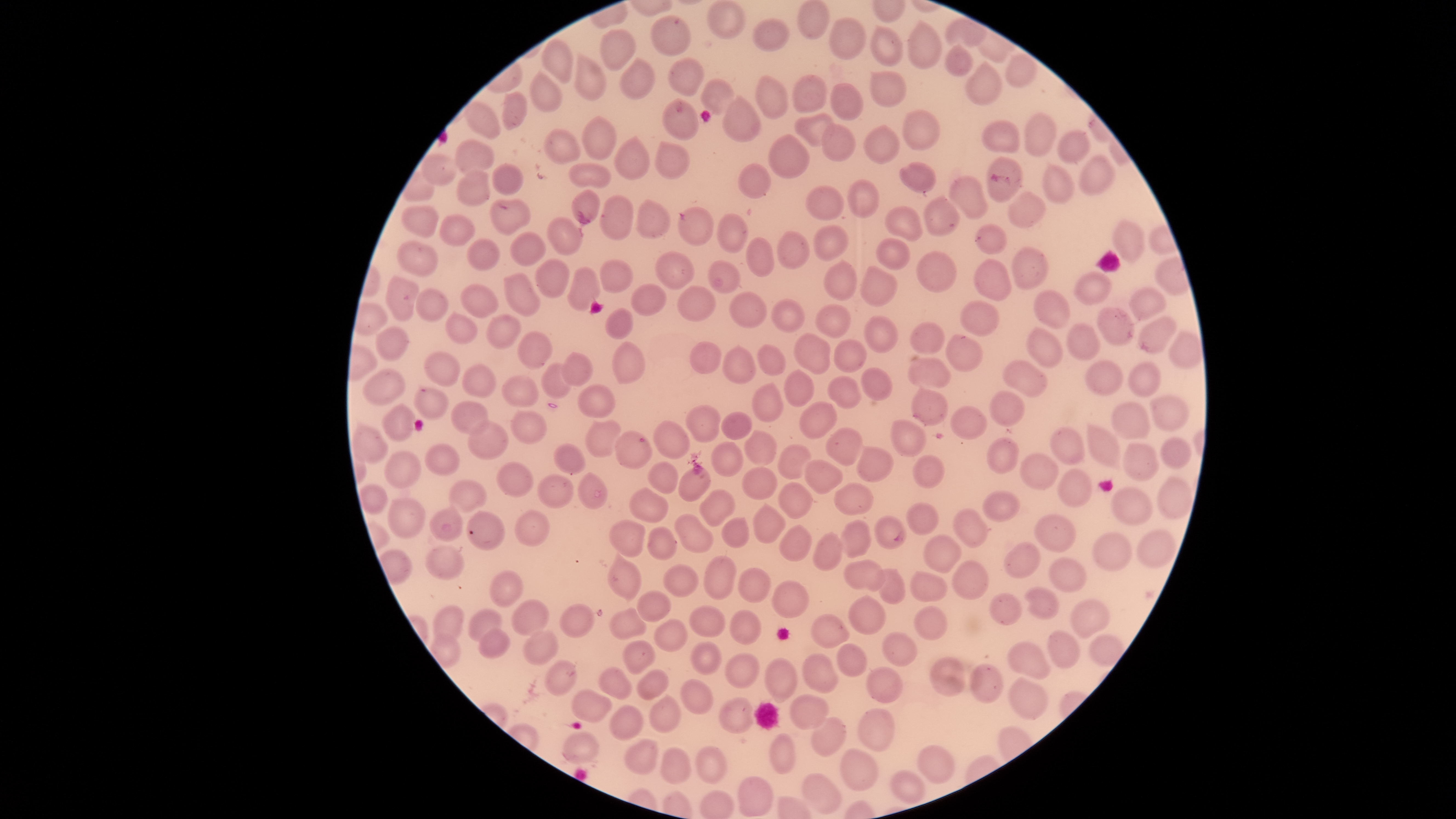

capture = smartphone photograph through the microscope eyepiece
image size = 1456×819 pixels
stain = Giemsa
species = Plasmodium falciparum
presence = malaria parasites seen
preparation = thin blood film
field of view = single
visible region = circular
parasitized red blood cells = approximate bounding boxes, in pixels from the top-left corner: (left=614, top=430, right=652, bottom=469), (left=874, top=516, right=907, bottom=549)
uninfected red blood cells = approximate bounding boxes, in pixels from the top-left corner: (left=797, top=1, right=831, bottom=40), (left=709, top=3, right=745, bottom=37), (left=652, top=16, right=688, bottom=56), (left=752, top=18, right=788, bottom=52), (left=828, top=18, right=865, bottom=59), (left=909, top=22, right=940, bottom=69), (left=869, top=26, right=903, bottom=66), (left=600, top=29, right=634, bottom=70), (left=542, top=39, right=574, bottom=85), (left=946, top=48, right=971, bottom=76), (left=574, top=55, right=605, bottom=101), (left=1006, top=55, right=1035, bottom=87), (left=668, top=58, right=703, bottom=98), (left=620, top=60, right=654, bottom=99), (left=967, top=64, right=1002, bottom=105), (left=870, top=70, right=906, bottom=107), (left=531, top=73, right=562, bottom=111), (left=793, top=74, right=828, bottom=113), (left=756, top=77, right=790, bottom=119), (left=701, top=80, right=733, bottom=115), (left=831, top=83, right=865, bottom=121), (left=503, top=92, right=528, bottom=131), (left=722, top=94, right=762, bottom=142), (left=665, top=100, right=697, bottom=140), (left=466, top=103, right=501, bottom=138), (left=905, top=109, right=940, bottom=151), (left=795, top=113, right=833, bottom=147), (left=1024, top=113, right=1055, bottom=157), (left=583, top=117, right=618, bottom=160), (left=982, top=121, right=1020, bottom=155), (left=823, top=123, right=855, bottom=163), (left=864, top=126, right=900, bottom=163), (left=546, top=129, right=581, bottom=162), (left=1057, top=129, right=1091, bottom=164), (left=768, top=133, right=809, bottom=178), (left=613, top=137, right=648, bottom=180), (left=456, top=141, right=494, bottom=173), (left=654, top=142, right=689, bottom=179), (left=422, top=154, right=456, bottom=186), (left=1078, top=157, right=1114, bottom=194), (left=987, top=158, right=1022, bottom=201), (left=492, top=163, right=523, bottom=194), (left=568, top=163, right=611, bottom=190), (left=901, top=163, right=936, bottom=193), (left=739, top=164, right=770, bottom=198), (left=1044, top=165, right=1073, bottom=204), (left=458, top=171, right=489, bottom=205), (left=949, top=177, right=989, bottom=220), (left=847, top=180, right=879, bottom=219), (left=805, top=186, right=845, bottom=219), (left=572, top=190, right=600, bottom=224), (left=1009, top=193, right=1045, bottom=227), (left=600, top=195, right=633, bottom=243), (left=926, top=197, right=960, bottom=236), (left=637, top=199, right=671, bottom=238), (left=401, top=204, right=441, bottom=236), (left=679, top=207, right=711, bottom=246), (left=884, top=208, right=921, bottom=241), (left=716, top=213, right=746, bottom=253), (left=440, top=216, right=474, bottom=245), (left=547, top=216, right=582, bottom=257), (left=1113, top=222, right=1145, bottom=261), (left=976, top=225, right=1006, bottom=254), (left=812, top=226, right=848, bottom=262), (left=777, top=231, right=809, bottom=270), (left=510, top=232, right=547, bottom=266), (left=747, top=238, right=773, bottom=276), (left=876, top=239, right=910, bottom=270), (left=467, top=240, right=501, bottom=272), (left=399, top=242, right=436, bottom=276), (left=1011, top=247, right=1049, bottom=290), (left=654, top=250, right=694, bottom=289), (left=917, top=252, right=957, bottom=291), (left=537, top=259, right=569, bottom=298), (left=974, top=259, right=1013, bottom=301), (left=598, top=260, right=633, bottom=292), (left=707, top=260, right=739, bottom=294), (left=825, top=260, right=857, bottom=301), (left=568, top=267, right=601, bottom=312), (left=860, top=267, right=897, bottom=305), (left=501, top=271, right=540, bottom=316), (left=1074, top=274, right=1111, bottom=305), (left=385, top=276, right=417, bottom=321), (left=631, top=284, right=666, bottom=315), (left=677, top=284, right=716, bottom=321), (left=459, top=285, right=498, bottom=318), (left=1130, top=288, right=1167, bottom=319), (left=416, top=289, right=447, bottom=322), (left=1035, top=291, right=1070, bottom=328), (left=728, top=293, right=766, bottom=326), (left=772, top=300, right=804, bottom=333), (left=959, top=301, right=999, bottom=336), (left=815, top=304, right=851, bottom=338), (left=605, top=308, right=631, bottom=339), (left=1096, top=308, right=1133, bottom=345), (left=446, top=315, right=477, bottom=344), (left=486, top=315, right=520, bottom=350), (left=1140, top=315, right=1178, bottom=353), (left=864, top=317, right=898, bottom=352), (left=911, top=323, right=946, bottom=355), (left=1067, top=326, right=1099, bottom=360), (left=376, top=327, right=408, bottom=360), (left=1028, top=328, right=1064, bottom=367), (left=1167, top=329, right=1201, bottom=368), (left=793, top=332, right=833, bottom=375), (left=517, top=333, right=552, bottom=370), (left=947, top=335, right=982, bottom=371), (left=834, top=339, right=868, bottom=372), (left=690, top=342, right=721, bottom=374), (left=612, top=343, right=643, bottom=384), (left=758, top=344, right=783, bottom=376), (left=722, top=347, right=755, bottom=384), (left=563, top=351, right=594, bottom=387), (left=424, top=353, right=460, bottom=387), (left=907, top=359, right=950, bottom=389), (left=1086, top=360, right=1122, bottom=394), (left=541, top=362, right=573, bottom=399), (left=1003, top=362, right=1049, bottom=398), (left=1129, top=364, right=1160, bottom=396), (left=461, top=365, right=494, bottom=399), (left=861, top=366, right=893, bottom=401), (left=783, top=369, right=815, bottom=406), (left=362, top=371, right=405, bottom=407), (left=502, top=374, right=540, bottom=408), (left=829, top=377, right=863, bottom=408), (left=751, top=384, right=783, bottom=421), (left=578, top=386, right=616, bottom=417), (left=415, top=387, right=448, bottom=419), (left=909, top=388, right=948, bottom=425), (left=989, top=391, right=1024, bottom=425), (left=1151, top=395, right=1188, bottom=432), (left=451, top=399, right=490, bottom=435), (left=799, top=401, right=835, bottom=439), (left=1114, top=403, right=1150, bottom=440), (left=383, top=405, right=413, bottom=442), (left=686, top=405, right=721, bottom=443), (left=949, top=407, right=986, bottom=438), (left=511, top=412, right=545, bottom=444), (left=720, top=413, right=752, bottom=439), (left=887, top=419, right=927, bottom=457), (left=466, top=421, right=507, bottom=459), (left=586, top=421, right=621, bottom=457), (left=653, top=422, right=691, bottom=458), (left=1086, top=422, right=1122, bottom=469), (left=352, top=425, right=388, bottom=463), (left=824, top=428, right=865, bottom=465), (left=1050, top=428, right=1088, bottom=465), (left=745, top=430, right=777, bottom=467), (left=987, top=436, right=1019, bottom=473), (left=1161, top=439, right=1190, bottom=469), (left=711, top=442, right=744, bottom=476), (left=778, top=442, right=813, bottom=479), (left=1123, top=443, right=1161, bottom=481), (left=553, top=444, right=585, bottom=475), (left=425, top=445, right=460, bottom=475), (left=855, top=446, right=894, bottom=482), (left=385, top=451, right=421, bottom=487), (left=1021, top=453, right=1058, bottom=490), (left=913, top=456, right=945, bottom=488), (left=802, top=459, right=842, bottom=493), (left=646, top=461, right=680, bottom=495), (left=497, top=463, right=535, bottom=498), (left=678, top=466, right=710, bottom=503), (left=742, top=467, right=777, bottom=499), (left=1058, top=468, right=1091, bottom=507), (left=577, top=473, right=606, bottom=510), (left=535, top=474, right=575, bottom=507), (left=1157, top=477, right=1195, bottom=521), (left=450, top=480, right=487, bottom=513), (left=836, top=482, right=874, bottom=516), (left=359, top=484, right=387, bottom=514), (left=779, top=484, right=813, bottom=518), (left=1109, top=487, right=1152, bottom=526), (left=630, top=488, right=669, bottom=523), (left=700, top=490, right=736, bottom=525), (left=981, top=492, right=1020, bottom=521), (left=388, top=499, right=424, bottom=539), (left=906, top=503, right=938, bottom=535), (left=751, top=505, right=785, bottom=544), (left=951, top=506, right=988, bottom=547), (left=429, top=508, right=465, bottom=543), (left=514, top=509, right=549, bottom=548), (left=466, top=512, right=505, bottom=549), (left=675, top=514, right=713, bottom=552), (left=1035, top=515, right=1076, bottom=552), (left=721, top=517, right=751, bottom=547), (left=609, top=520, right=647, bottom=559), (left=840, top=520, right=871, bottom=559), (left=779, top=525, right=813, bottom=561), (left=648, top=526, right=677, bottom=562), (left=1139, top=529, right=1176, bottom=568), (left=1093, top=533, right=1132, bottom=570), (left=813, top=534, right=843, bottom=570), (left=924, top=534, right=962, bottom=575), (left=1002, top=543, right=1043, bottom=577), (left=426, top=547, right=466, bottom=580), (left=380, top=549, right=411, bottom=585), (left=608, top=555, right=641, bottom=601), (left=704, top=555, right=737, bottom=598), (left=953, top=559, right=987, bottom=600), (left=1049, top=559, right=1086, bottom=592), (left=845, top=560, right=885, bottom=592), (left=663, top=565, right=698, bottom=597), (left=491, top=568, right=524, bottom=606), (left=737, top=568, right=772, bottom=603), (left=877, top=569, right=905, bottom=604), (left=910, top=571, right=947, bottom=602), (left=773, top=580, right=809, bottom=618), (left=1025, top=587, right=1059, bottom=619), (left=638, top=590, right=671, bottom=622), (left=990, top=594, right=1021, bottom=624), (left=848, top=597, right=884, bottom=635), (left=1071, top=599, right=1109, bottom=638), (left=512, top=600, right=549, bottom=636), (left=559, top=603, right=595, bottom=638), (left=913, top=606, right=947, bottom=641), (left=435, top=607, right=463, bottom=643), (left=688, top=607, right=725, bottom=637), (left=611, top=609, right=647, bottom=641), (left=729, top=609, right=762, bottom=646), (left=470, top=610, right=502, bottom=642), (left=811, top=615, right=849, bottom=647), (left=654, top=620, right=688, bottom=652), (left=479, top=630, right=510, bottom=659), (left=523, top=631, right=558, bottom=664), (left=1048, top=631, right=1079, bottom=668), (left=882, top=633, right=916, bottom=667), (left=1088, top=635, right=1123, bottom=668), (left=623, top=641, right=656, bottom=674), (left=690, top=642, right=721, bottom=674), (left=838, top=642, right=867, bottom=678), (left=1006, top=642, right=1050, bottom=679), (left=726, top=653, right=761, bottom=689), (left=803, top=654, right=837, bottom=693), (left=766, top=659, right=795, bottom=702), (left=931, top=659, right=965, bottom=697), (left=547, top=661, right=577, bottom=695), (left=969, top=665, right=1001, bottom=702), (left=599, top=668, right=632, bottom=699), (left=867, top=668, right=902, bottom=701), (left=636, top=669, right=669, bottom=701), (left=1008, top=678, right=1046, bottom=720), (left=679, top=680, right=713, bottom=715), (left=571, top=690, right=611, bottom=722), (left=788, top=693, right=829, bottom=728), (left=648, top=695, right=681, bottom=732), (left=721, top=699, right=753, bottom=733), (left=611, top=706, right=641, bottom=739), (left=857, top=709, right=894, bottom=753), (left=809, top=717, right=845, bottom=758), (left=561, top=730, right=598, bottom=763), (left=770, top=736, right=794, bottom=775), (left=625, top=739, right=660, bottom=775), (left=917, top=745, right=955, bottom=784), (left=662, top=748, right=691, bottom=784), (left=696, top=749, right=725, bottom=782), (left=841, top=749, right=877, bottom=792), (left=892, top=771, right=923, bottom=802), (left=803, top=775, right=841, bottom=813), (left=739, top=777, right=770, bottom=817)